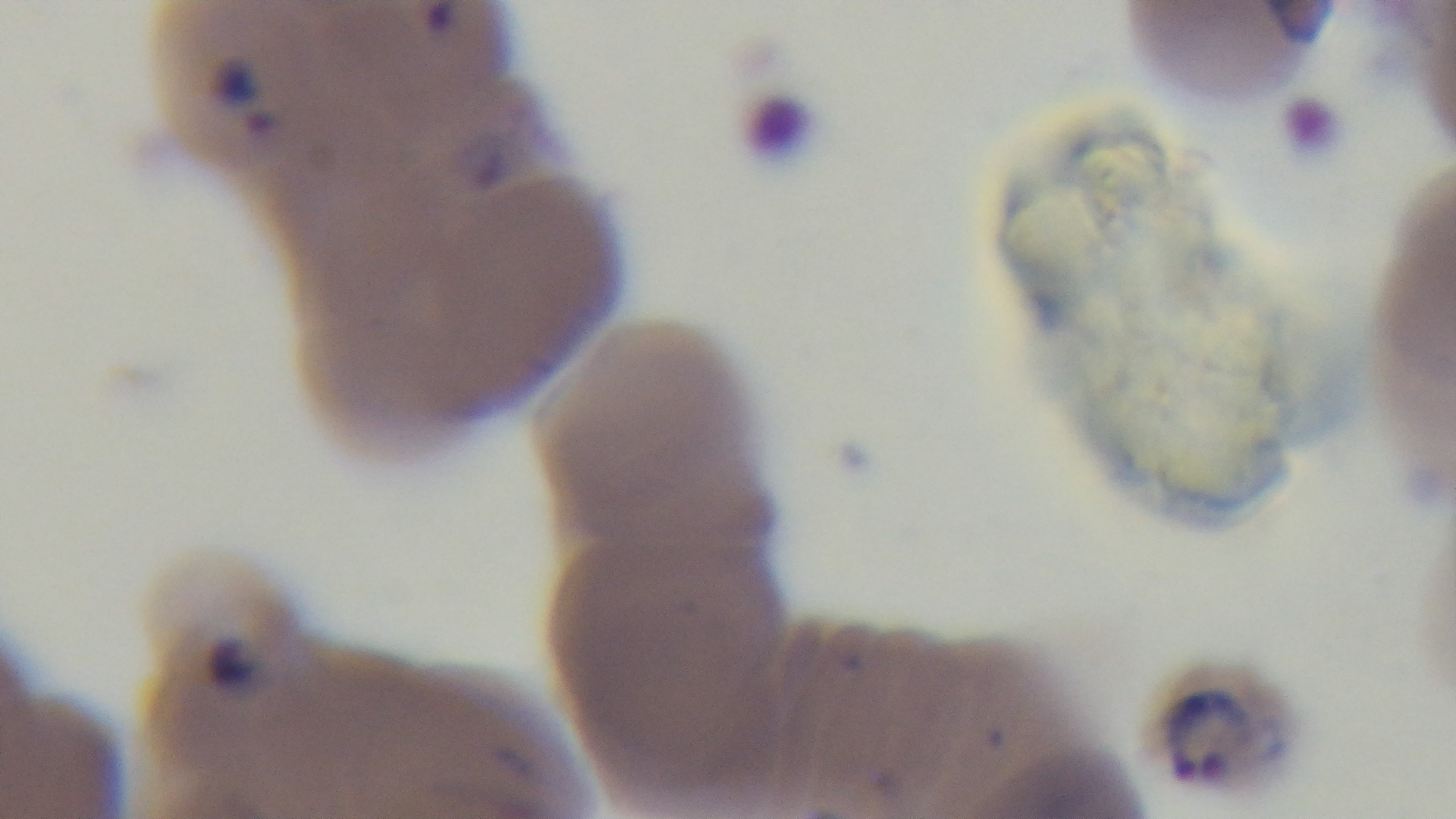
Summary:
  - Preparation: thin blood film
  - Stain: Giemsa
  - Capture: mounted 4K digital camera
  - Modality: light microscopy
  - Malaria status: positive
  - Field of view: one from the slide
  - Objective: 100x oil immersion